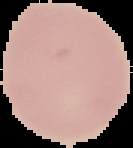
Image is 133×148 pixels. Cell region segmented out of the field of view; the surrounding area is masked to black. From a thin blood smear. Result: no Plasmodium parasites detected.